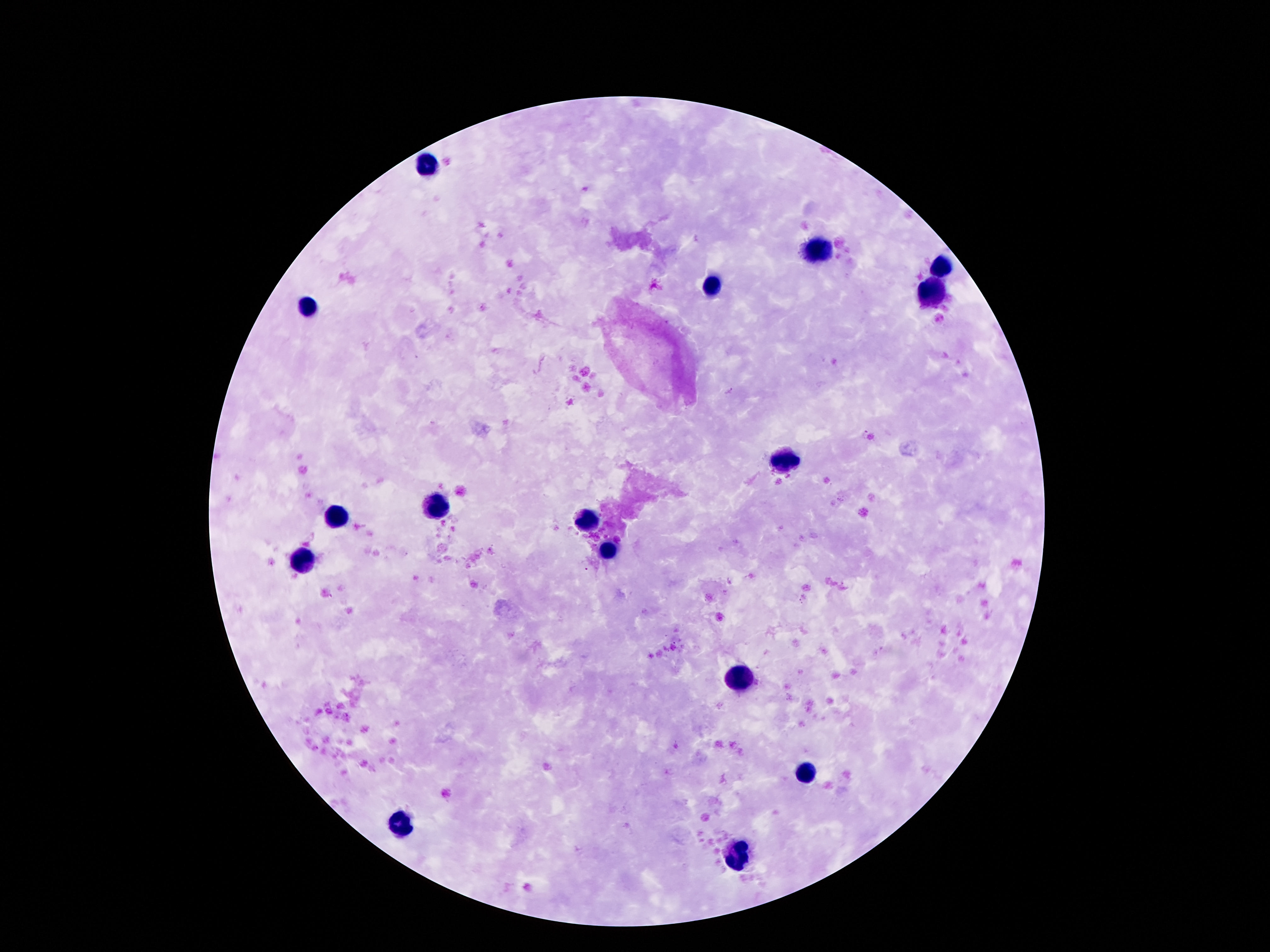
Approximate centers as [x, y] in pixels.
Summary:
  - Leukocyte locations: [423, 165], [815, 248], [941, 269], [711, 283], [929, 292], [307, 308], [783, 465], [435, 506], [337, 518], [587, 521], [607, 553], [301, 562], [737, 676], [805, 774], [399, 828], [737, 853]
  - Image size: 1270×952 pixels
  - Field of view: single
  - Capture: smartphone camera through the microscope eyepiece
  - Magnification: 100x
  - Preparation: thick blood film
  - Patient malaria status: not infected
  - Stain: Giemsa